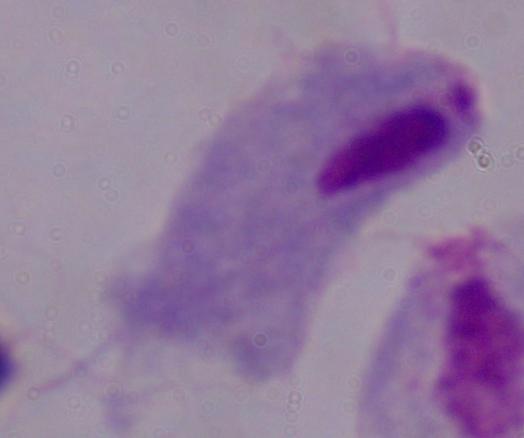

Summary:
  - Modality: micrograph
  - Magnification: 1000x
  - Identification: trichomonad